Give the preparation type.
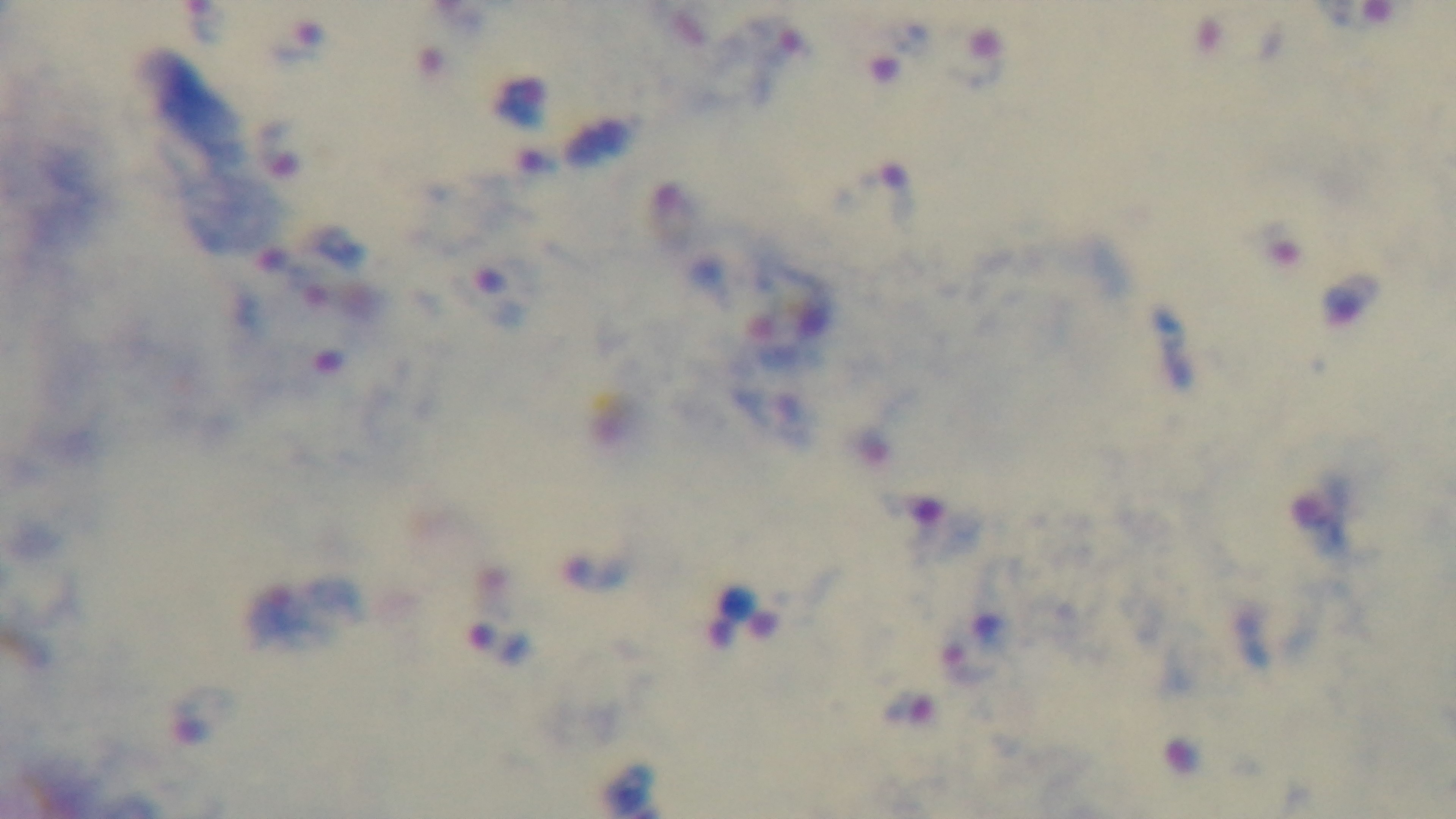
It is a thick blood film.

Summary:
  - Objective: 100x oil immersion
  - Field of view: single
  - Capture: mounted 4K digital camera
  - Stain: Giemsa
  - Malaria status: infected
  - Modality: light microscopy